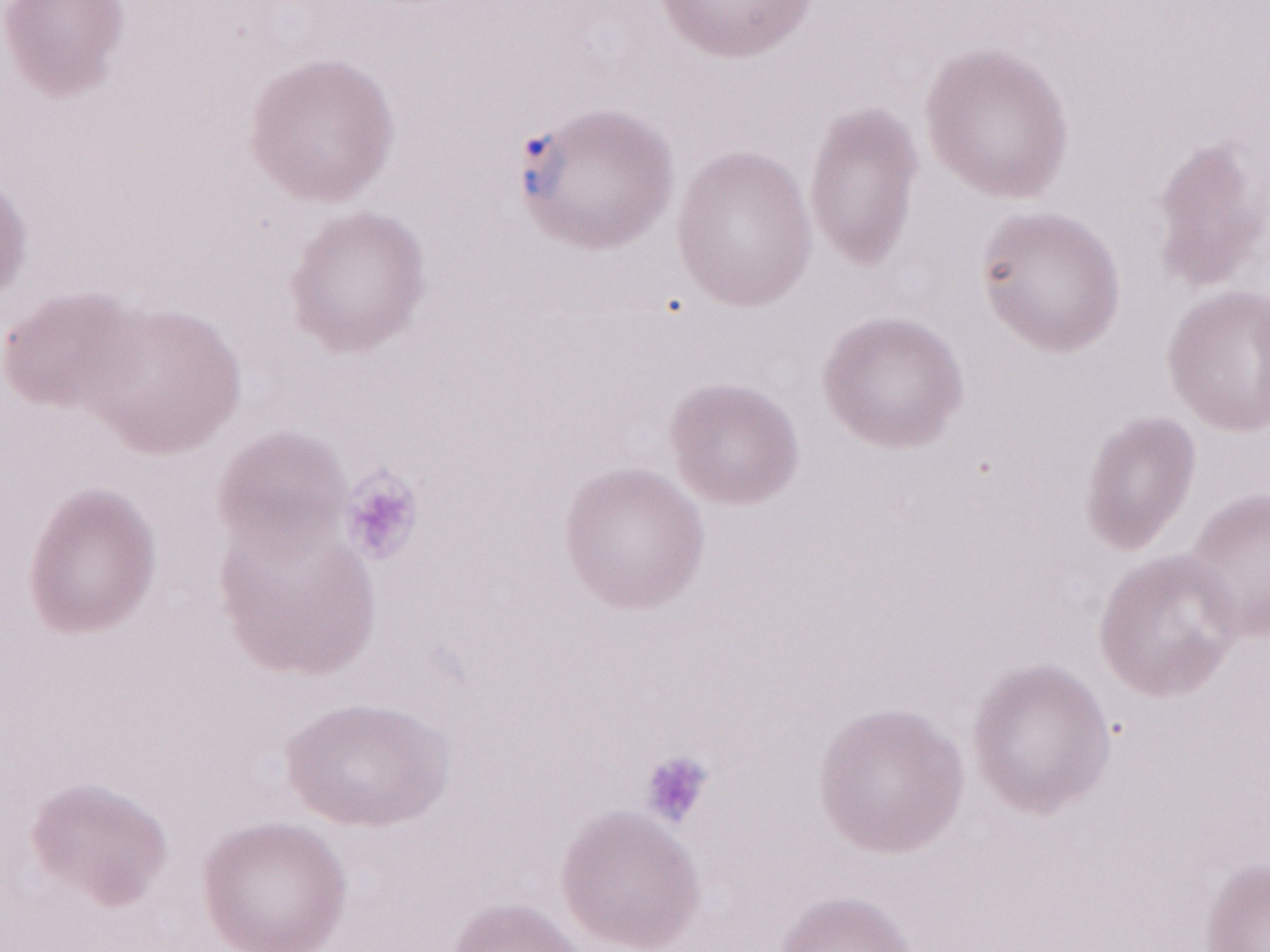
Olympus BX43 microscope and DP73 digital camera. One field of this slide. Thin blood film. Magnification: 1,000x. Patient diagnosis: malaria infection. Image is 1270×952 pixels. May-Grünwald-Giemsa stain.